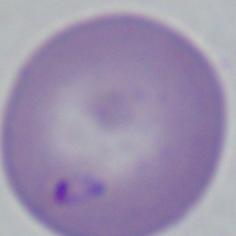
identification = Babesia
magnification = 1000x
modality = photomicrograph